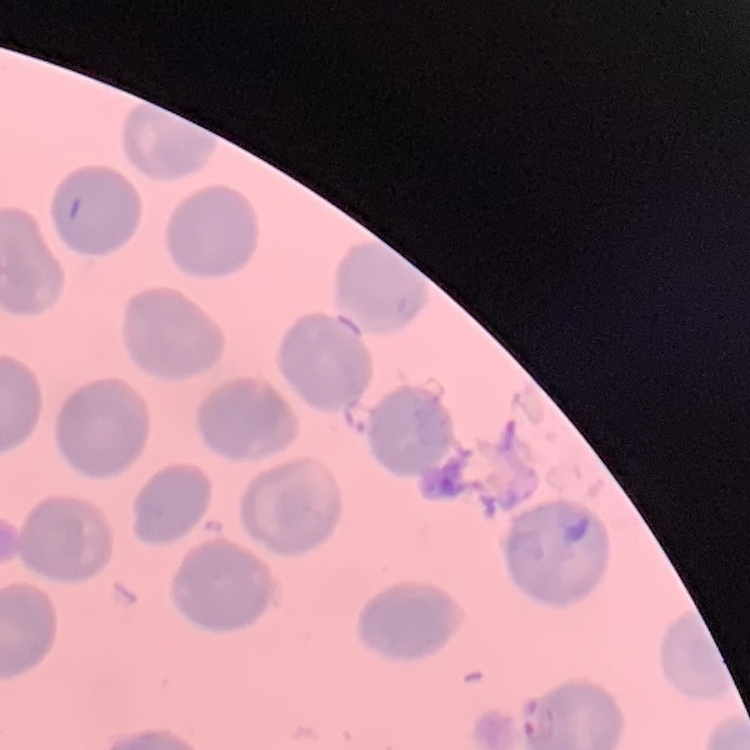

erythrocyte morphology = no rouleaux formation
preparation = thin peripheral smear
stain = Field's or Giemsa
image type = square crop of a larger photomicrograph